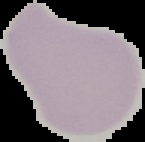
Segmented cell region on a black background. From a thin blood film. Image is 145×142 pixels. Malaria status: uninfected.